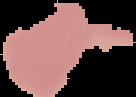

image type = segmented cell region on a black background
preparation = thin blood film
image size = 136×97 pixels
result = negative for Plasmodium parasites